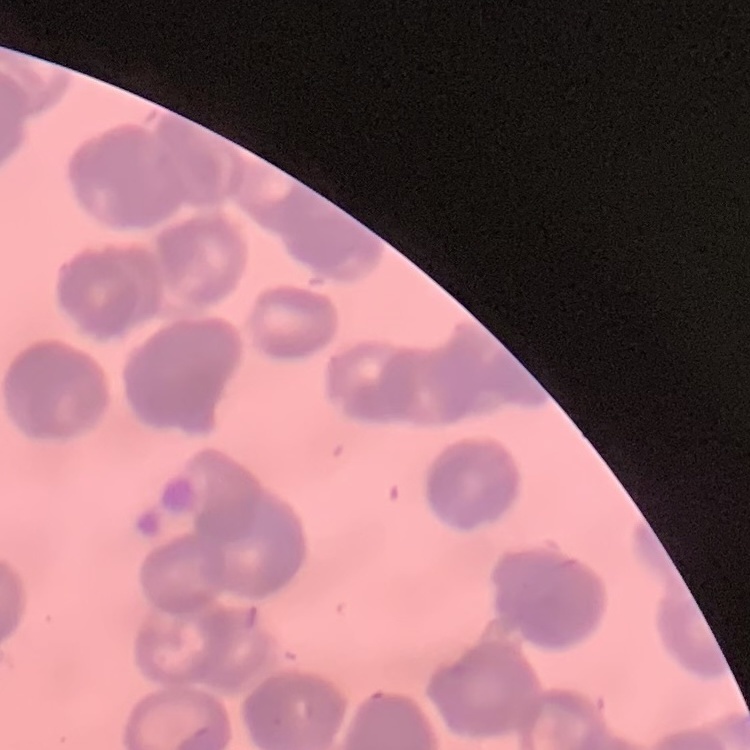

Summary:
  - Erythrocyte morphology: rouleaux formation
  - Image type: one tile cut from a larger photomicrograph
  - Preparation: thin blood smear
  - Stain: Field's or Giemsa